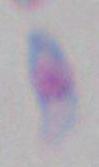

modality = micrograph
identification = Toxoplasma gondii
magnification = 1000x